Classify this cell by malaria status.
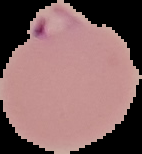
Parasitized.

preparation = thin blood smear
image size = 142×154 pixels
image type = cell region segmented out of the field of view; surrounding area masked to black